Mark where leukocytes are.
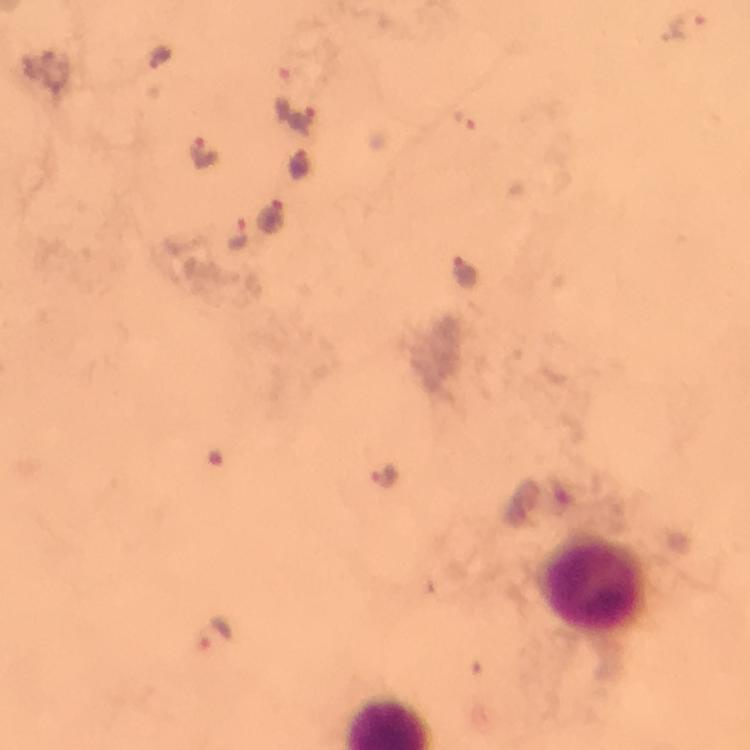

Approximate centers as (x, y) in pixels.
Leukocytes: (594, 584).

Summary:
  - Malaria parasite locations: (687, 29), (158, 55), (302, 119), (203, 151), (297, 164), (270, 216), (238, 234), (467, 275), (389, 477), (210, 637)
  - Image size: 750×750 pixels
  - Context: from a malaria diagnostic workup
  - Preparation: thick blood smear
  - Stain: Giemsa
  - Capture: smartphone mounted on the microscope
  - Immersion oil: used
  - Magnification: 100x
  - Cropped from: a single field of view